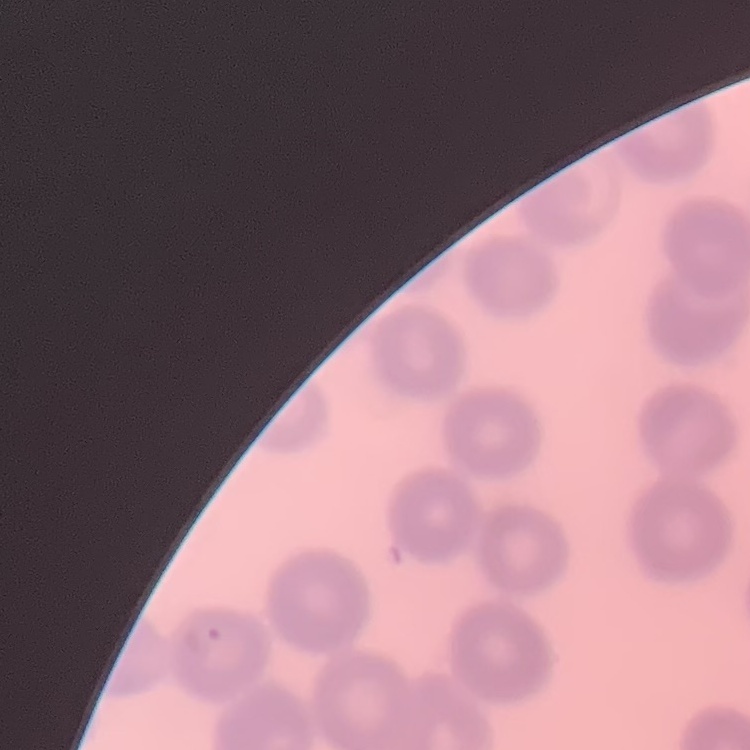
red blood cell morphology = no rouleaux formation
stain = Field's or Giemsa
preparation = thin peripheral smear
image type = square crop of a larger photomicrograph